State which cell type is depicted.
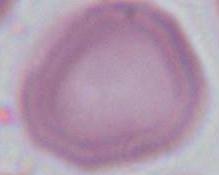

An erythrocyte.

Micrograph. Captured at 1000x magnification.